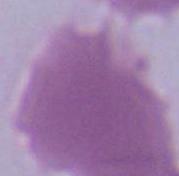
magnification = 1000x
modality = photomicrograph
identification = erythrocyte